Point out each malaria parasite.
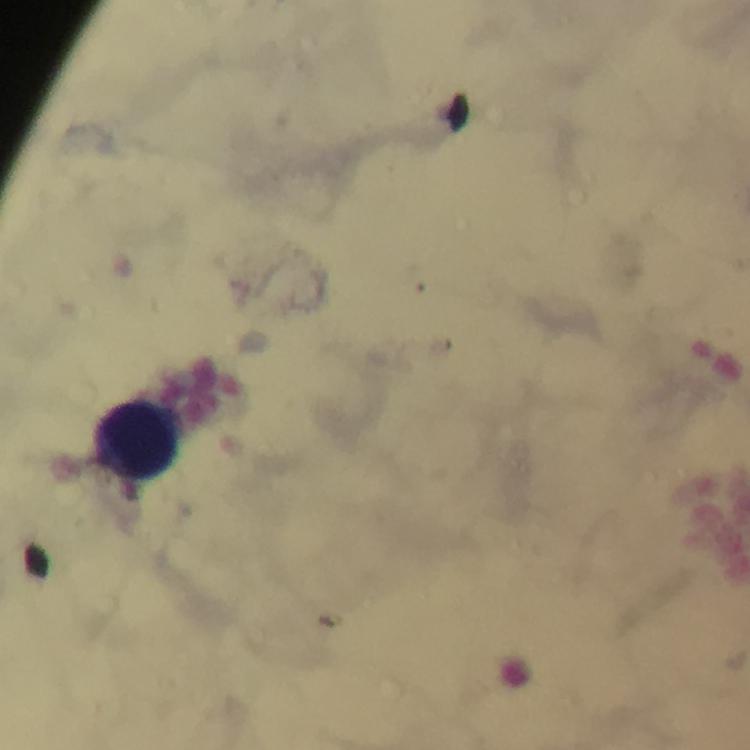
No malaria parasites seen.

Approximate centers as (x, y) in pixels.
Summary:
  - Leukocyte locations: (141, 439)
  - Cropped from: a single field of view
  - Context: from a diagnostic examination for malaria
  - Stain: Giemsa
  - Preparation: thick blood smear
  - Immersion oil: applied
  - Magnification: 100x
  - Capture: smartphone mounted on the microscope
  - Image size: 750×750 pixels